Name the parasite shown.
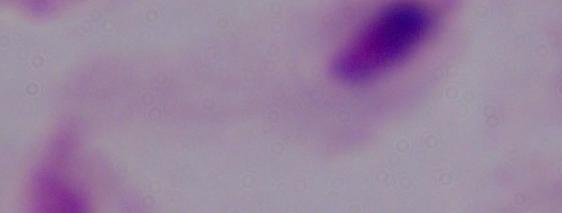

A trichomonad.

modality = micrograph
magnification = 1000x